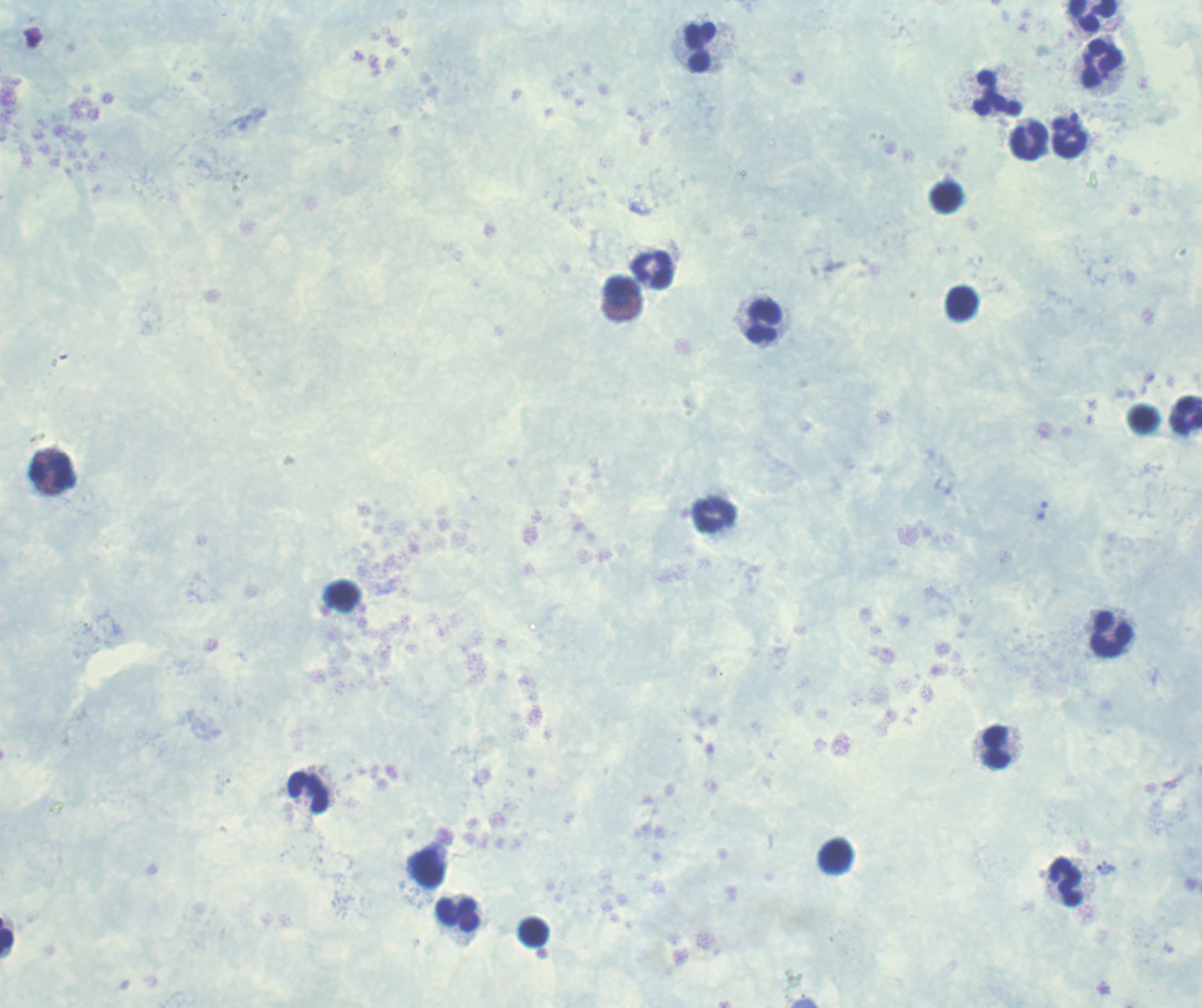 Approximate centers as (x, y) in pixels. Leukocyte locations: (1093, 17), (700, 47), (1102, 65), (998, 93), (1070, 138), (1029, 141), (652, 270), (623, 292), (962, 303), (763, 323), (1186, 416), (49, 471), (714, 515), (1111, 633), (996, 747), (307, 792), (427, 869), (1066, 882), (457, 914), (533, 932), (6, 936). Trophozoite locations: (1106, 869). Image is 1202×1008 pixels. Romanowsky stain. Thick blood film. Previously used in an actual diagnosis. Result: Plasmodium parasites identified. One field from this slide. Background quality: unsatisfactory. Captured at 100x magnification.